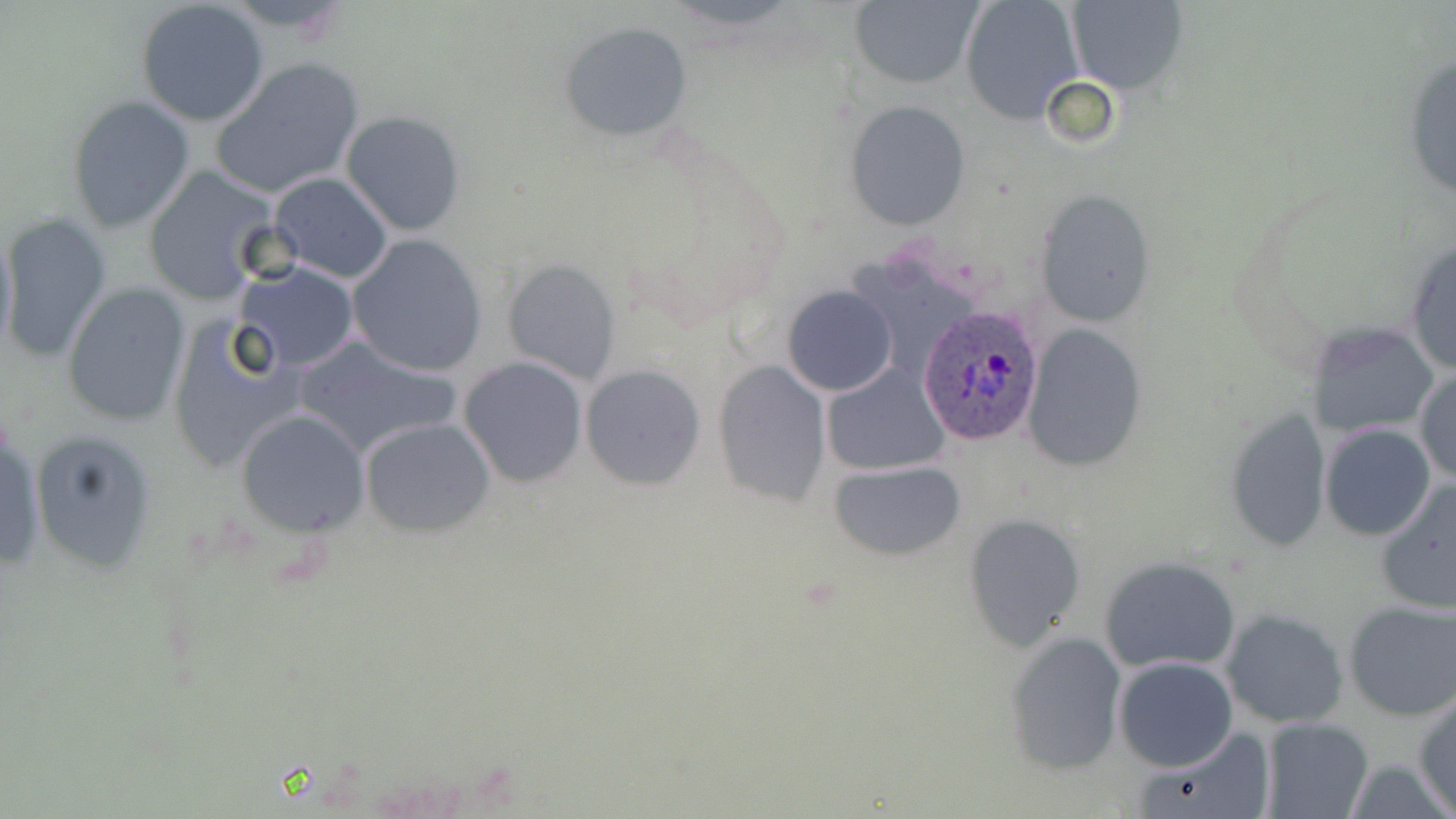

slide-level diagnosis = Plasmodium ovale
image size = 1456×819 pixels
Plasmodium ovale-infected red blood cell locations = approximate bounding boxes as (x1,y1)-(x2,y2) corner pairs in pixels: (916,305)-(1046,450)
modality = light microscopy
uninfected red blood cell locations = approximate bounding boxes as (x1,y1)-(x2,y2) corner pairs in pixels: (136,0)-(270,127), (220,0)-(361,35), (848,0)-(980,90), (959,0)-(1084,122), (1064,0)-(1188,95), (559,21)-(693,143), (1401,51)-(1456,208), (212,56)-(365,198), (1041,77)-(1119,150), (66,94)-(196,234), (843,101)-(970,231), (340,110)-(468,237), (142,164)-(280,303), (266,170)-(394,283), (1035,191)-(1156,326), (2,214)-(115,365), (0,220)-(17,363), (346,234)-(487,378), (1403,236)-(1456,378), (503,259)-(621,385), (231,261)-(362,373), (61,283)-(192,428), (782,285)-(898,396), (166,314)-(304,474), (1307,320)-(1441,439), (1020,322)-(1146,474), (293,337)-(463,460), (458,356)-(588,489), (714,359)-(831,507), (823,363)-(950,478), (580,364)-(704,491), (1415,366)-(1456,484), (236,410)-(369,536), (1225,410)-(1333,552), (0,414)-(43,579), (359,418)-(495,537), (1320,423)-(1436,541), (30,426)-(157,575), (830,460)-(965,560), (1374,477)-(1456,614), (964,513)-(1086,650), (1097,555)-(1242,674), (1342,598)-(1456,722), (1220,608)-(1350,730), (1006,630)-(1127,775), (1112,657)-(1237,771), (1413,692)-(1456,815), (1259,715)-(1374,819), (1134,724)-(1276,819)
field of view = one of a larger specimen
preparation = thin blood film
magnification = 1000x
stain = May-Grünwald-Giemsa